Classify this cell by malaria status.
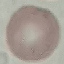
Uninfected.

Summary:
  - Capture: smartphone through the microscope eyepiece
  - Preparation: thin blood film
  - Image type: cell patch, automatically extracted from a larger field of view and resized to 64 × 64 pixels
  - Stain: Giemsa